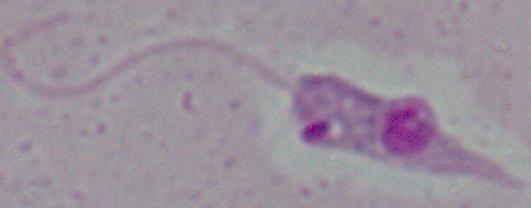

{
  "identification": "Leishmania",
  "magnification": "1000x",
  "modality": "micrograph"
}